State the preparation type.
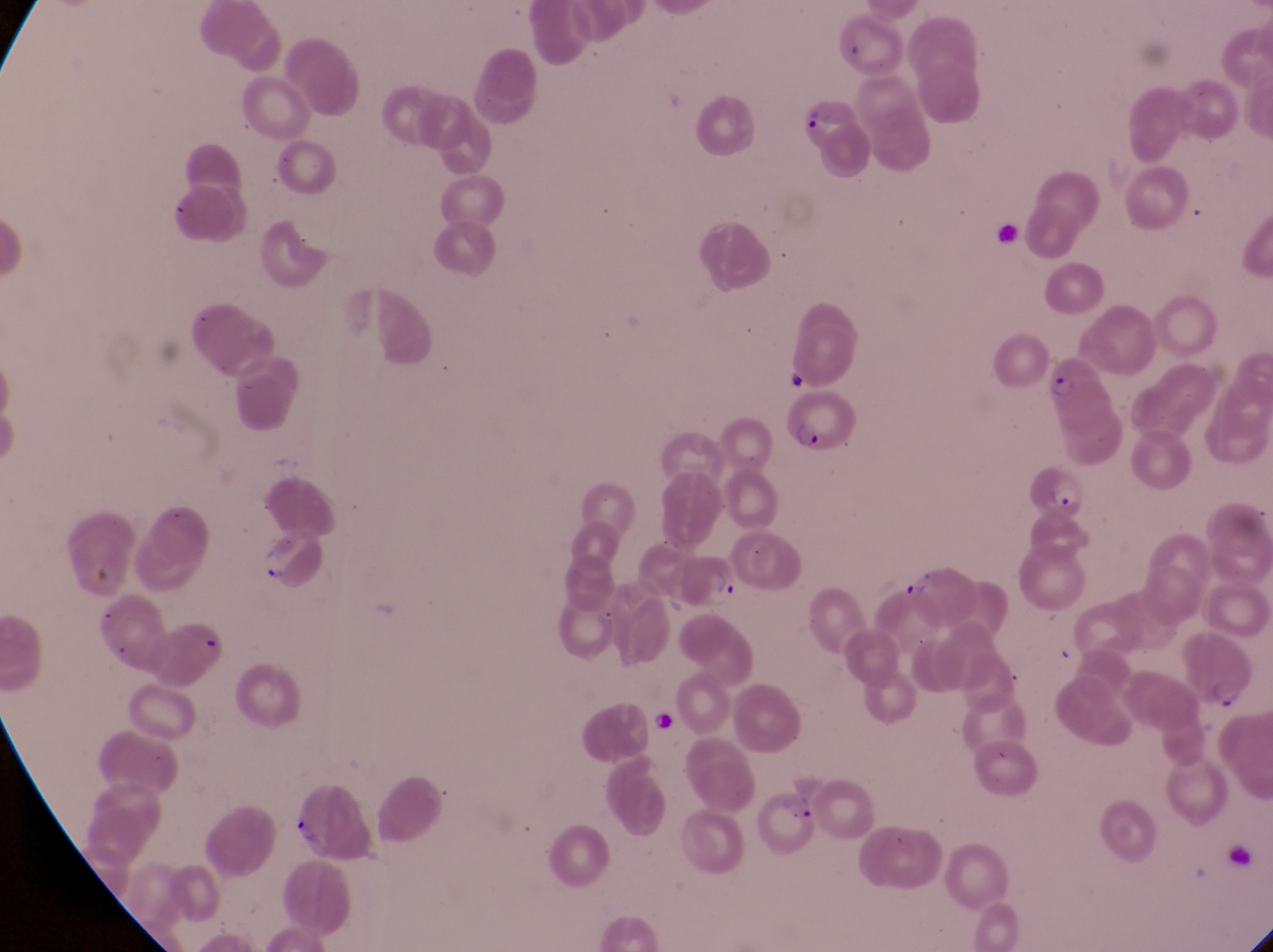
Thin blood smear.

artifact (platelet-like body, stain precipitate, or debris) locations = approximate bounding boxes as [left, top, right, bottom] in pixels: [83, 561, 120, 588], [652, 707, 684, 747]
trophozoite locations = approximate bounding boxes as [left, top, right, bottom] in pixels: [254, 542, 289, 585]
image size = 1273×952 pixels
capture = smartphone photograph through the eyepiece of an Olympus CX-23 microscope
magnification = 1000x
field of view = single
parasitised red blood cell locations = approximate bounding boxes as [left, top, right, bottom] in pixels: [794, 90, 863, 152], [1044, 354, 1107, 421], [781, 392, 859, 457], [1013, 460, 1087, 523], [677, 550, 739, 613], [901, 559, 979, 629], [155, 621, 229, 684], [1179, 629, 1255, 705], [764, 784, 826, 851]
country = Uganda